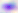 Toxoplasma gondii is seen. Photomicrograph. 400x magnification.